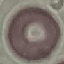

{
  "malaria_status": "uninfected",
  "capture": "smartphone camera at the microscope eyepiece",
  "image_type": "automatically extracted cell patch, resized to 64 × 64 pixels",
  "stain": "Giemsa",
  "preparation": "thin smear"
}